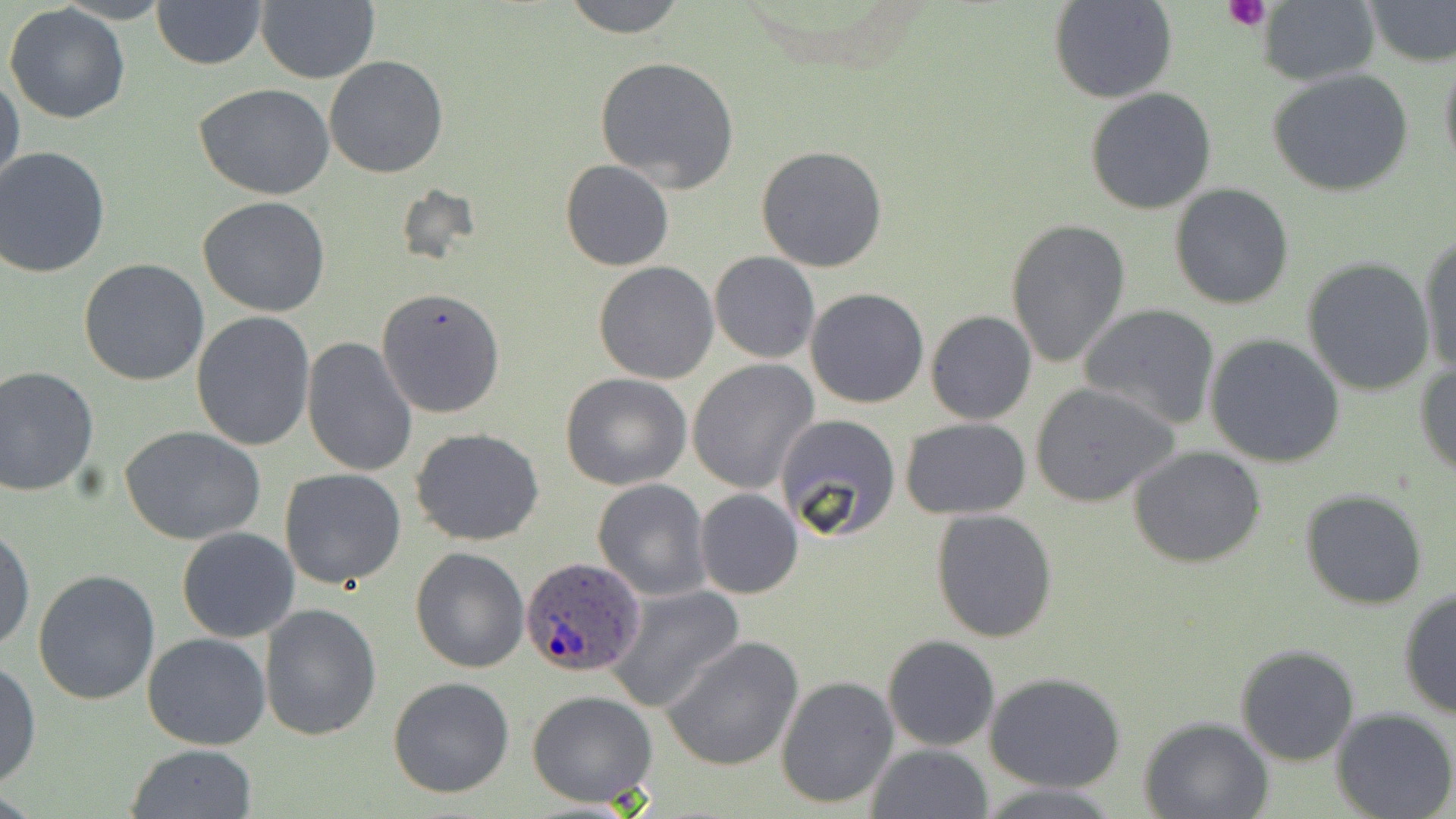

{
  "slide_level_diagnosis": "Plasmodium ovale",
  "platelet_locations": "approximate bounding boxes as [x1, y1, x2, y2] in pixels: [1224, 0, 1272, 31]",
  "image_size": "1456×819 pixels",
  "field_of_view": "one of a larger specimen",
  "stain": "May-Grünwald-Giemsa",
  "plasmodium_ovale_infected_red_blood_cell_locations": "approximate bounding boxes as [x1, y1, x2, y2] in pixels: [519, 555, 645, 678]",
  "modality": "light microscopy",
  "preparation": "thin blood film",
  "magnification": "1000x",
  "uninfected_red_blood_cell_locations": "approximate bounding boxes as [x1, y1, x2, y2] in pixels: [255, 0, 379, 84], [560, 0, 689, 38], [1049, 0, 1179, 104], [1258, 0, 1380, 85], [1363, 0, 1456, 67], [152, 1, 265, 70], [3, 3, 130, 123], [1438, 50, 1456, 182], [324, 54, 449, 178], [594, 55, 739, 192], [1268, 67, 1414, 197], [0, 71, 25, 196], [194, 83, 338, 201], [1084, 87, 1218, 214], [756, 143, 888, 273], [0, 147, 110, 278], [559, 158, 674, 271], [1168, 184, 1295, 311], [197, 195, 332, 316], [1004, 216, 1133, 368], [1418, 233, 1456, 380], [709, 251, 820, 363], [1302, 257, 1438, 397], [78, 258, 210, 387], [593, 261, 720, 385], [376, 287, 506, 418], [804, 288, 931, 409], [1077, 304, 1221, 430], [189, 310, 314, 451], [925, 310, 1036, 427], [1204, 334, 1349, 468], [300, 335, 418, 477], [687, 359, 819, 494], [1415, 361, 1456, 481], [0, 365, 101, 497], [561, 373, 692, 491], [1029, 381, 1180, 507], [773, 413, 902, 542], [900, 418, 1032, 520], [119, 426, 265, 544], [411, 427, 546, 546], [1128, 445, 1267, 569], [279, 468, 407, 589], [592, 478, 712, 601], [695, 488, 804, 599], [1300, 488, 1430, 610], [930, 509, 1058, 644], [0, 525, 35, 654], [176, 527, 301, 643], [409, 545, 529, 673], [33, 569, 162, 705], [607, 585, 744, 712], [1398, 588, 1456, 719], [260, 602, 382, 742], [142, 633, 271, 750], [882, 634, 999, 751], [662, 635, 805, 771], [1233, 644, 1360, 767], [0, 659, 40, 789], [984, 672, 1129, 793], [774, 674, 900, 810], [388, 675, 515, 798], [527, 690, 658, 808], [1330, 705, 1456, 819], [1139, 716, 1275, 819], [126, 743, 259, 818], [866, 743, 994, 819], [973, 779, 1122, 817]"
}